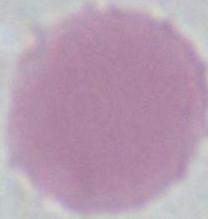

Photomicrograph. 1000x magnification. A red blood cell is seen.